State the blood parasite species.
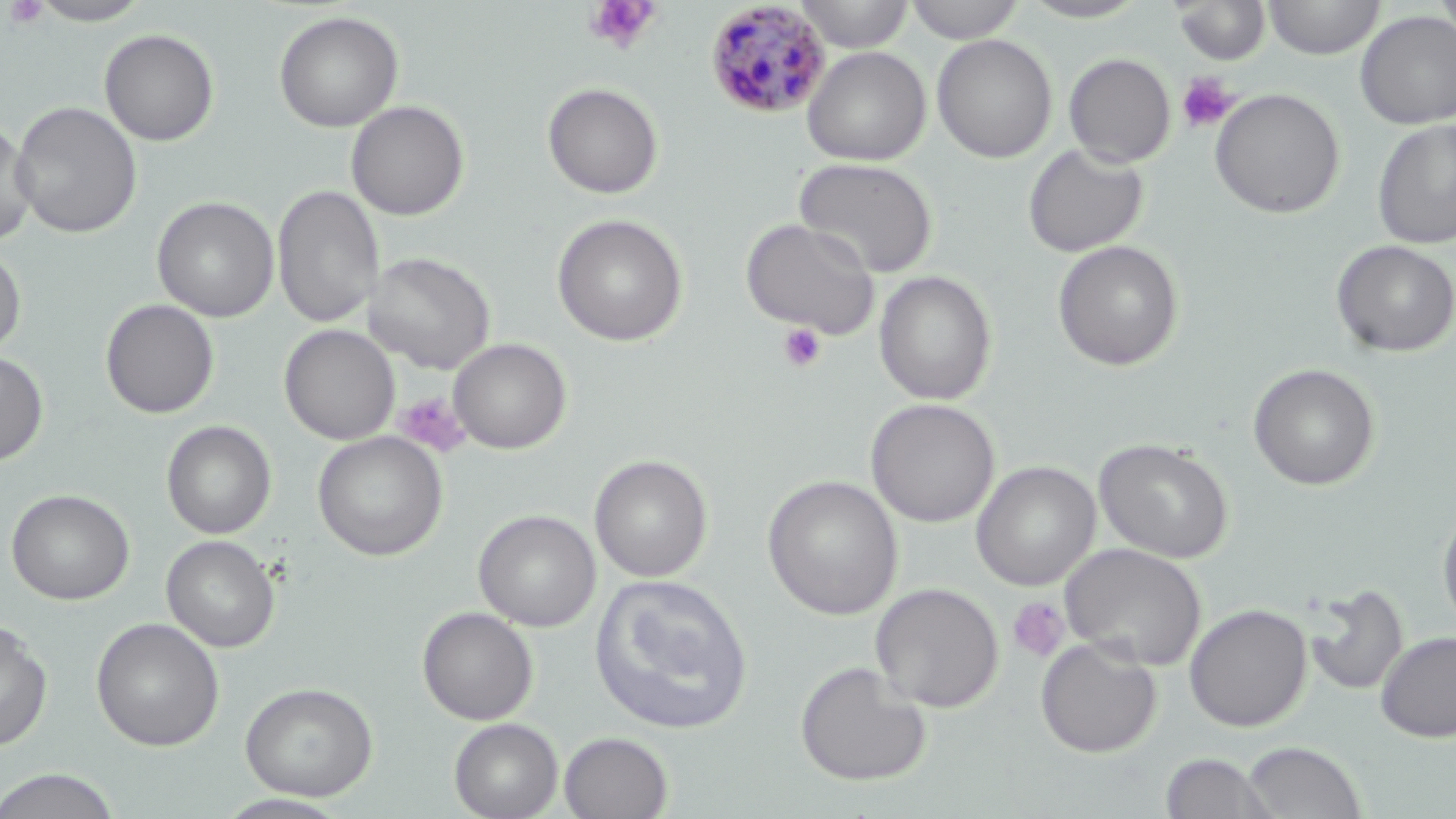

Plasmodium malariae.

Approximate bounding boxes as (x1, y1, x2, y2) in pixels. Plasmodium malariae-infected red blood cell locations: (704, 2, 832, 119). Platelet locations: (4, 0, 50, 30), (583, 1, 662, 55), (1176, 72, 1238, 133), (777, 322, 828, 372), (393, 392, 470, 458), (1007, 597, 1072, 664). Uninfected red blood cell locations: (27, 0, 155, 26), (794, 0, 915, 53), (905, 0, 1025, 43), (1019, 0, 1149, 22), (1265, 0, 1384, 60), (1435, 0, 1456, 49), (1173, 1, 1271, 65), (273, 10, 404, 133), (1355, 11, 1456, 129), (99, 28, 219, 146), (932, 34, 1057, 163), (802, 46, 931, 166), (1063, 53, 1176, 168), (542, 82, 663, 198), (1210, 88, 1345, 219), (10, 100, 142, 238), (346, 100, 469, 221), (1372, 118, 1456, 250), (0, 120, 38, 250), (1023, 143, 1148, 258), (793, 157, 938, 278), (273, 185, 383, 330), (152, 197, 279, 322), (552, 213, 688, 347), (741, 217, 880, 337), (1052, 240, 1184, 371), (1331, 241, 1456, 358), (0, 242, 26, 359), (364, 251, 494, 374), (873, 270, 997, 405), (100, 299, 218, 419), (280, 325, 400, 445), (448, 338, 571, 454), (0, 352, 49, 465), (1248, 363, 1379, 490), (865, 398, 999, 527), (162, 420, 277, 539), (312, 431, 448, 561), (1094, 439, 1234, 562), (589, 454, 712, 582), (971, 461, 1100, 591), (763, 475, 903, 620), (6, 489, 134, 605), (1437, 502, 1456, 635), (474, 509, 600, 632), (162, 535, 280, 652), (1059, 543, 1207, 670), (589, 574, 754, 735), (1305, 581, 1408, 697), (870, 583, 1004, 713), (1184, 603, 1313, 732), (417, 606, 538, 725), (0, 617, 53, 750), (91, 617, 224, 751), (1375, 631, 1456, 743), (1035, 637, 1162, 758), (794, 661, 932, 787), (239, 681, 378, 801), (449, 718, 563, 819), (559, 731, 673, 818), (1242, 741, 1367, 819), (1159, 752, 1278, 819), (0, 768, 123, 819), (215, 793, 353, 818). 1000x magnification. Light microscopy. May-Grünwald-Giemsa stain. Thin blood smear. Image is 1456×819 pixels. One field of a larger specimen.